Assess this cell for malaria.
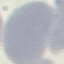

Uninfected.

Thin blood smear. Giemsa-stained preparation. Cell patch, automatically extracted from a larger field of view and resized to 64 × 64 pixels. Acquired by smartphone through the microscope eyepiece.